Locate every Plasmodium parasite and every leukocyte.
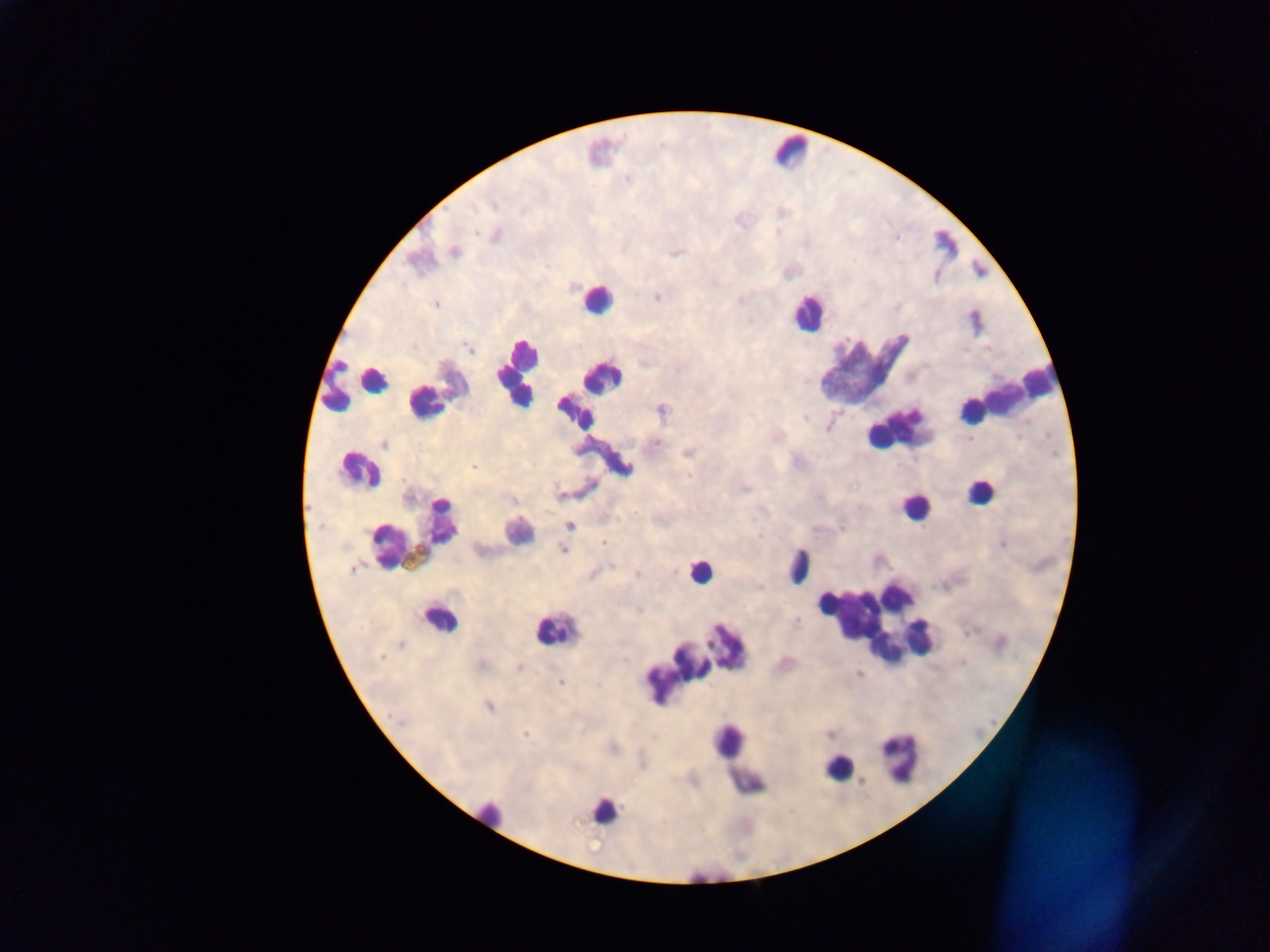
Approximate centers as x y in pixels.
Plasmodium parasites: 494 234; 453 252; 676 252; 656 296; 435 303; 469 348; 661 410; 971 439; 384 443; 654 443; 687 452; 474 467; 744 487; 560 495; 513 500; 568 525; 604 542; 1002 543; 563 549; 636 573; 518 666; 560 682; 488 705; 526 733; 829 734; 612 747.
Leukocytes: 789 151; 945 243; 597 299; 807 312; 862 367; 516 371; 602 377; 373 380; 360 385; 335 387; 435 393; 1007 394; 575 412; 897 429; 358 470; 981 491; 915 506; 413 529; 518 531; 798 565; 699 571; 439 619; 878 620; 555 630; 915 637; 920 639; 705 651; 666 678; 728 740; 900 756; 838 766; 749 782; 603 810; 490 813; 707 875.

image size = 1270×952 pixels
capture = mobile-phone photograph through a microscope
country = Ghana
preparation = thick blood smear
field of view = single